State the preparation type.
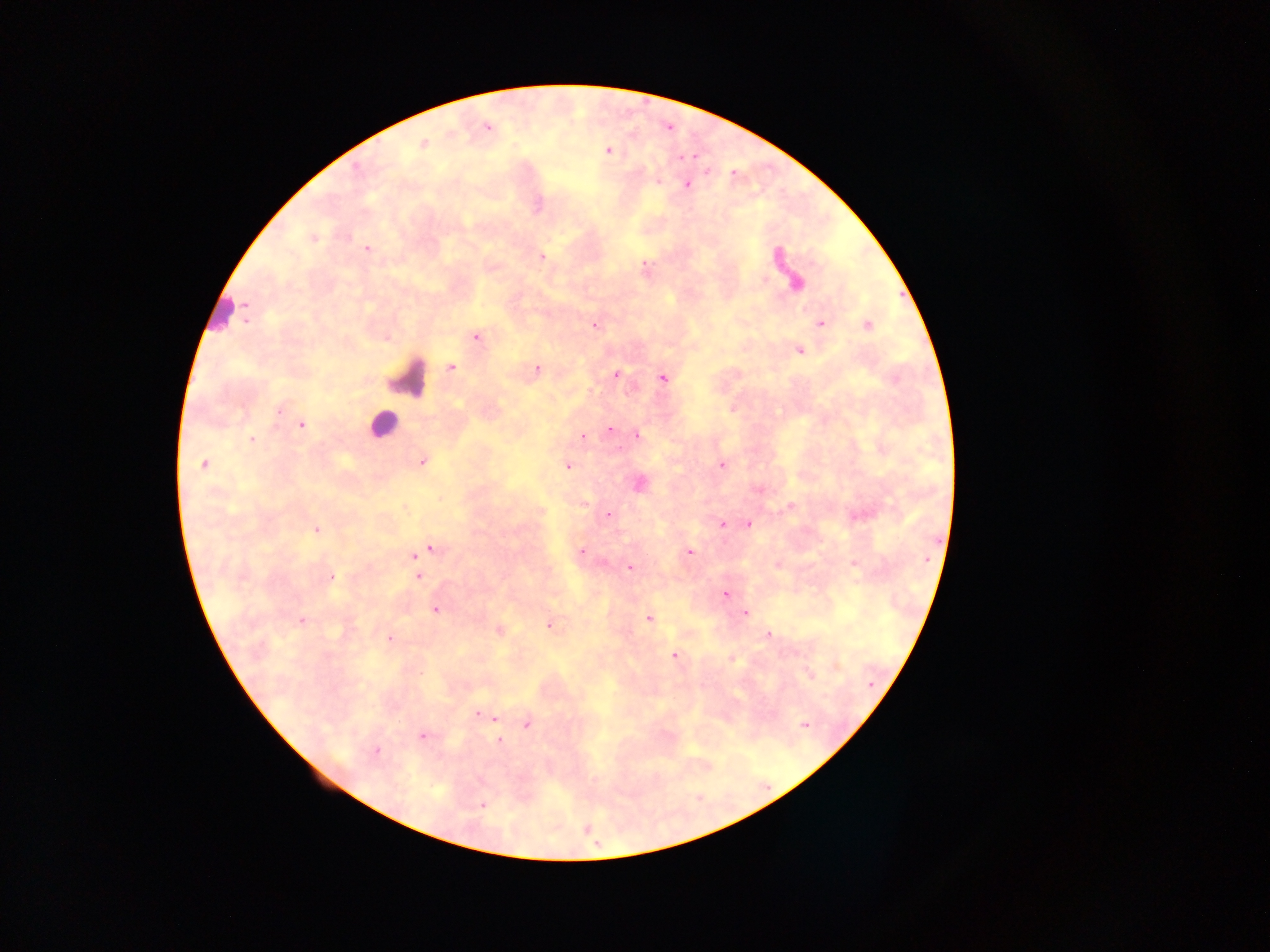
Thick blood film.

Approximate centers as [x, y] in pixels. Leukocyte locations: [220, 311], [406, 377], [383, 424]. Malaria parasite locations: [487, 128], [423, 144], [607, 150], [657, 180], [686, 184], [312, 238], [366, 248], [541, 257], [795, 282], [821, 323], [868, 324], [595, 325], [476, 336], [799, 350], [450, 367], [536, 369], [615, 375], [662, 378], [279, 408], [301, 425], [609, 430], [637, 435], [583, 436], [251, 439], [421, 461], [204, 463], [722, 464], [567, 465], [638, 483], [541, 512], [608, 515], [748, 523], [722, 524], [316, 530], [429, 548], [581, 550], [688, 551], [414, 556], [777, 564], [854, 564], [629, 567], [417, 570], [417, 576], [330, 577], [725, 594], [435, 609], [745, 613], [648, 617], [302, 621], [549, 624], [498, 630], [768, 635], [389, 638], [674, 655], [731, 658], [810, 676], [483, 714], [492, 718], [527, 723], [804, 724], [422, 734], [498, 740], [375, 752], [482, 804]. Image is 1270×952 pixels. Single field of view. Collected in Ghana. Mobile-phone photograph taken through the microscope.